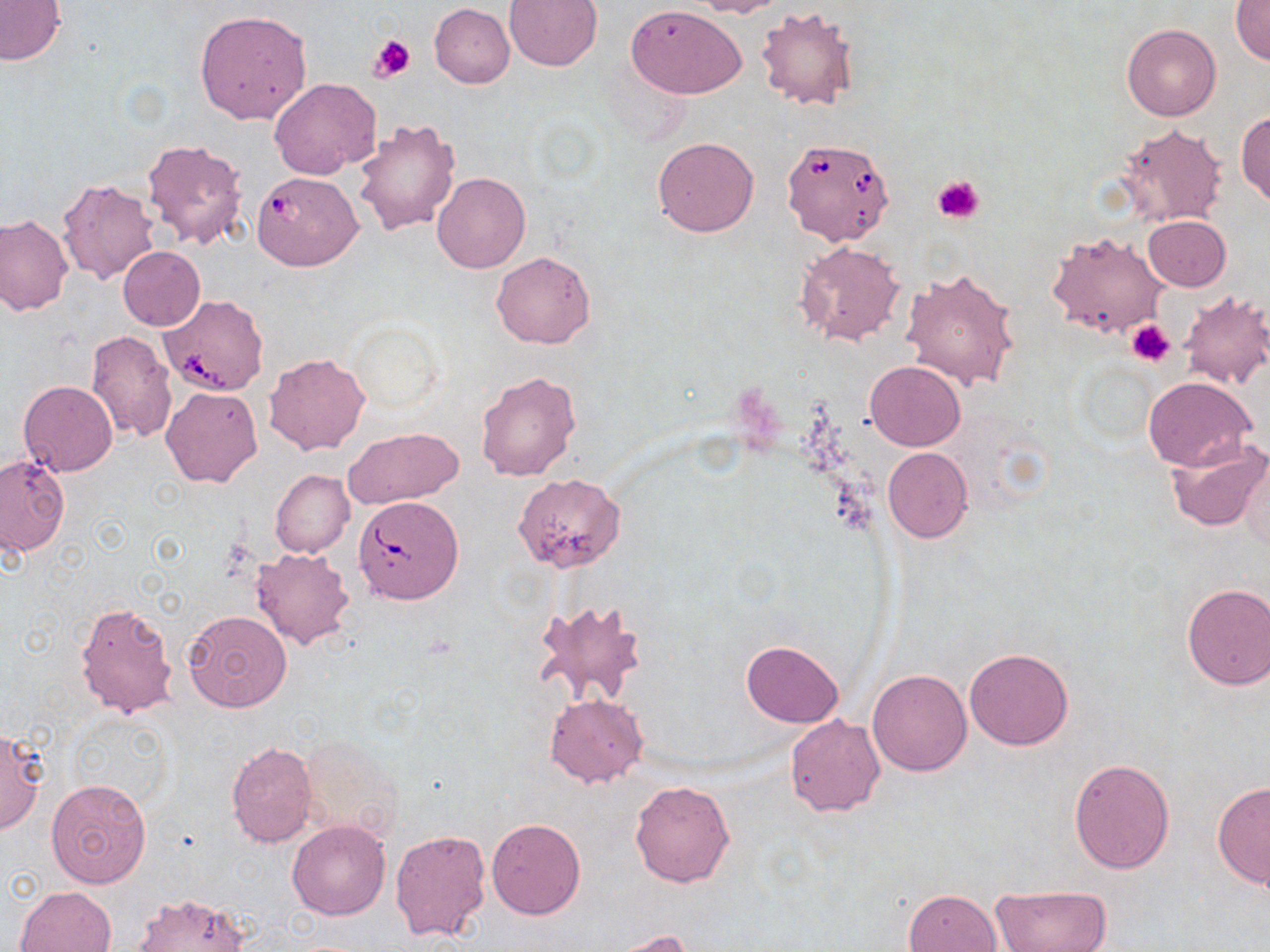
Summary:
  - Coordinate format: approximate bounding boxes as named x1/y1/x2/y2 corners in pixels
  - Babesia divergens-infected red blood cell locations: (x1=777, y1=141, x2=898, y2=250), (x1=253, y1=170, x2=364, y2=271), (x1=158, y1=294, x2=269, y2=396), (x1=354, y1=494, x2=462, y2=604)
  - Platelet locations: (x1=369, y1=34, x2=415, y2=83), (x1=932, y1=174, x2=986, y2=224), (x1=1125, y1=319, x2=1175, y2=366)
  - Uninfected red blood cell locations: (x1=505, y1=0, x2=603, y2=70), (x1=690, y1=0, x2=785, y2=18), (x1=0, y1=1, x2=66, y2=66), (x1=1232, y1=2, x2=1270, y2=67), (x1=430, y1=3, x2=514, y2=87), (x1=627, y1=5, x2=746, y2=98), (x1=755, y1=6, x2=860, y2=111), (x1=195, y1=10, x2=312, y2=125), (x1=1122, y1=24, x2=1221, y2=121), (x1=269, y1=78, x2=381, y2=179), (x1=1237, y1=111, x2=1270, y2=208), (x1=353, y1=118, x2=461, y2=237), (x1=1115, y1=121, x2=1228, y2=227), (x1=652, y1=137, x2=760, y2=237), (x1=142, y1=138, x2=250, y2=252), (x1=432, y1=173, x2=530, y2=274), (x1=57, y1=178, x2=160, y2=286), (x1=0, y1=214, x2=73, y2=316), (x1=1142, y1=215, x2=1230, y2=291), (x1=1044, y1=229, x2=1170, y2=339), (x1=793, y1=240, x2=906, y2=348), (x1=118, y1=246, x2=204, y2=331), (x1=490, y1=250, x2=597, y2=348), (x1=903, y1=266, x2=1020, y2=391), (x1=1177, y1=292, x2=1270, y2=389), (x1=87, y1=330, x2=178, y2=443), (x1=265, y1=354, x2=370, y2=456), (x1=865, y1=360, x2=965, y2=450), (x1=476, y1=369, x2=583, y2=482), (x1=1142, y1=376, x2=1256, y2=472), (x1=18, y1=380, x2=118, y2=477), (x1=161, y1=385, x2=262, y2=487), (x1=342, y1=428, x2=463, y2=510), (x1=1164, y1=436, x2=1268, y2=533), (x1=882, y1=447, x2=972, y2=542), (x1=1, y1=457, x2=69, y2=556), (x1=1236, y1=457, x2=1269, y2=550), (x1=270, y1=469, x2=353, y2=557), (x1=512, y1=473, x2=625, y2=572), (x1=251, y1=548, x2=355, y2=649), (x1=1181, y1=583, x2=1270, y2=690), (x1=538, y1=598, x2=649, y2=706), (x1=74, y1=600, x2=178, y2=720), (x1=183, y1=610, x2=290, y2=713), (x1=740, y1=640, x2=843, y2=727), (x1=963, y1=648, x2=1073, y2=750), (x1=866, y1=669, x2=972, y2=776), (x1=543, y1=692, x2=650, y2=789), (x1=784, y1=714, x2=887, y2=817), (x1=0, y1=729, x2=47, y2=836), (x1=297, y1=732, x2=404, y2=840), (x1=227, y1=741, x2=318, y2=846), (x1=1069, y1=758, x2=1175, y2=874), (x1=46, y1=777, x2=153, y2=889), (x1=629, y1=780, x2=736, y2=887), (x1=1213, y1=781, x2=1270, y2=889), (x1=486, y1=818, x2=585, y2=920), (x1=287, y1=819, x2=391, y2=920), (x1=389, y1=828, x2=491, y2=942), (x1=990, y1=884, x2=1111, y2=951), (x1=14, y1=886, x2=116, y2=951), (x1=903, y1=887, x2=1002, y2=952), (x1=133, y1=893, x2=249, y2=951), (x1=606, y1=930, x2=697, y2=952)
  - Slide-level diagnosis: Babesia divergens
  - Modality: light microscopy
  - Preparation: thin blood smear
  - Image size: 1270×952 pixels
  - Magnification: 1000x
  - Field of view: one of a larger specimen
  - Stain: May-Grünwald-Giemsa